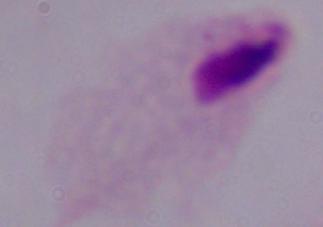
modality: micrograph
identification: trichomonad
magnification: 1000x